Assess this cell for malaria.
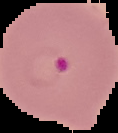
It is parasitized.

image size = 118×133 pixels
image type = segmented cell region on a black background
preparation = thin blood smear